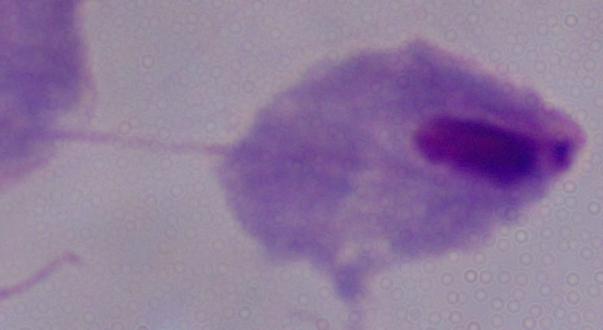
Summary:
  - Magnification: 1000x
  - Identification: trichomonad
  - Modality: micrograph